Comment on the morphology of the erythrocytes.
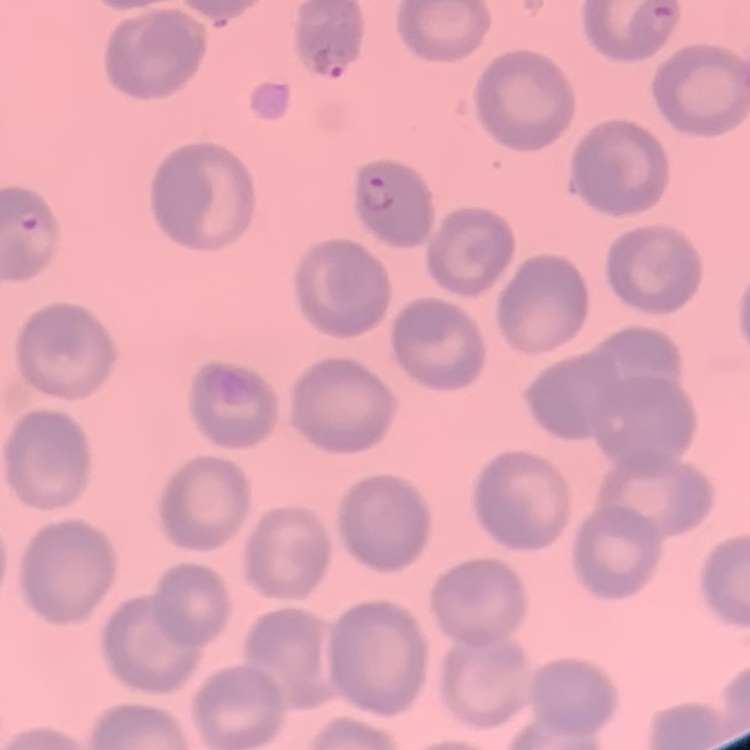

No rouleaux formation.

{
  "stain": "Field's or Giemsa",
  "image_type": "one tile cut from a larger photomicrograph",
  "preparation": "thin peripheral smear"
}